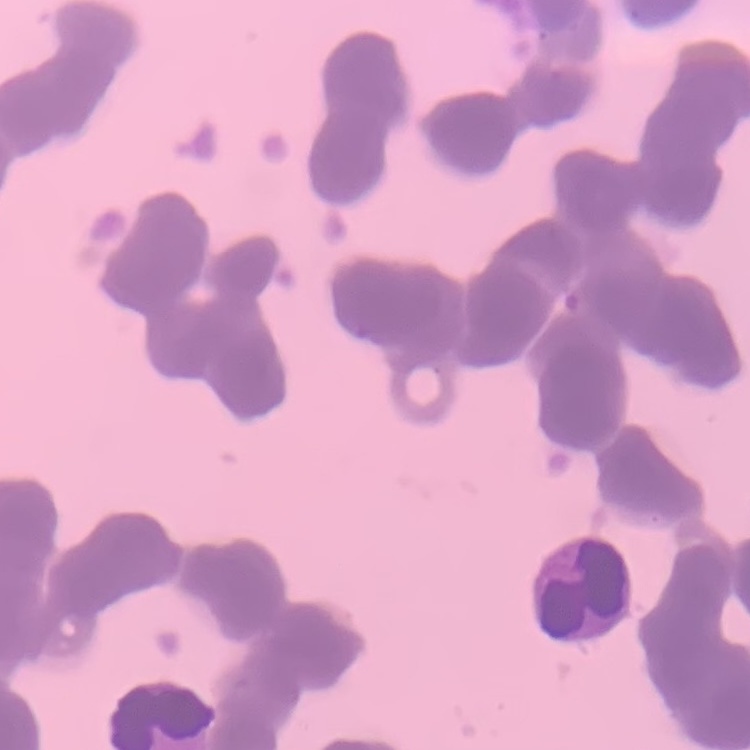
Summary:
  - Red blood cell morphology: rouleaux formation
  - Preparation: thin blood film
  - Image type: one tile cut from a larger photomicrograph
  - Stain: Field's or Giemsa